Locate malaria parasites and leukocytes.
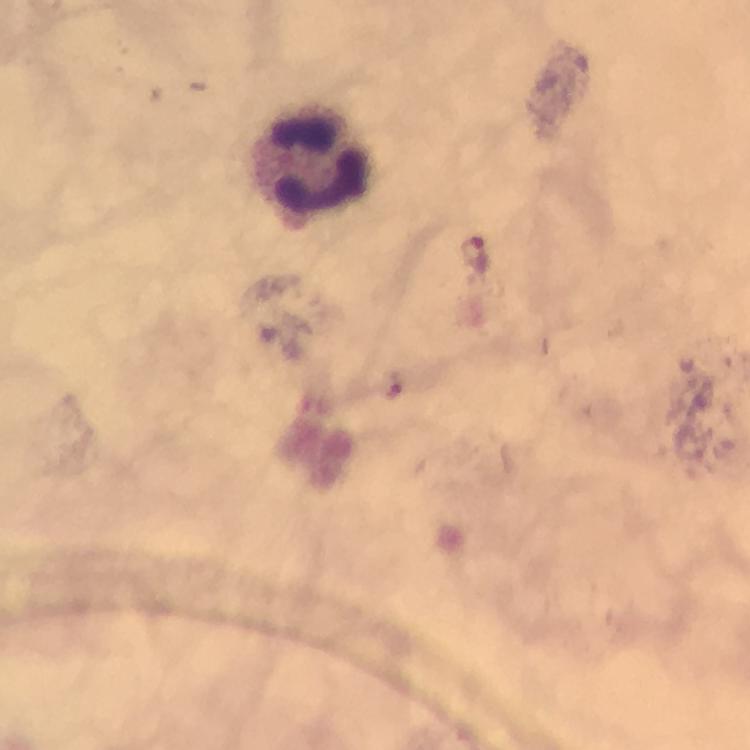

Approximate centers as [x, y] in pixels.
Malaria parasites: [474, 258].
Leukocytes: [316, 159].

context = from a diagnostic examination for malaria
preparation = thick smear
stain = Giemsa
image size = 750×750 pixels
capture = smartphone camera through the microscope
magnification = 100x
immersion oil = used
cropped from = a single field of view